Comment on the morphology of the erythrocytes.
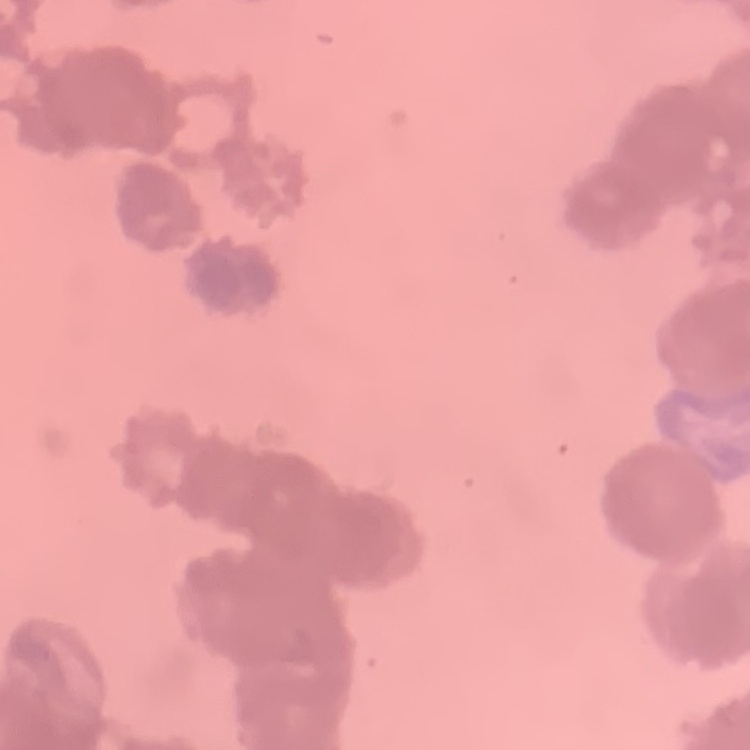
They show rouleaux formation.

Stained with either Field's or Giemsa. Square crop of a larger photomicrograph. Thin blood film.